State which cell type is depicted.
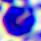

This is a leukocyte.

Summary:
  - Magnification: 400x
  - Modality: photomicrograph